Assess this cell for malaria.
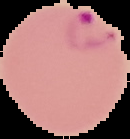
It is parasitized.

image type = segmented cell region on a black background
preparation = thin blood film
image size = 130×139 pixels